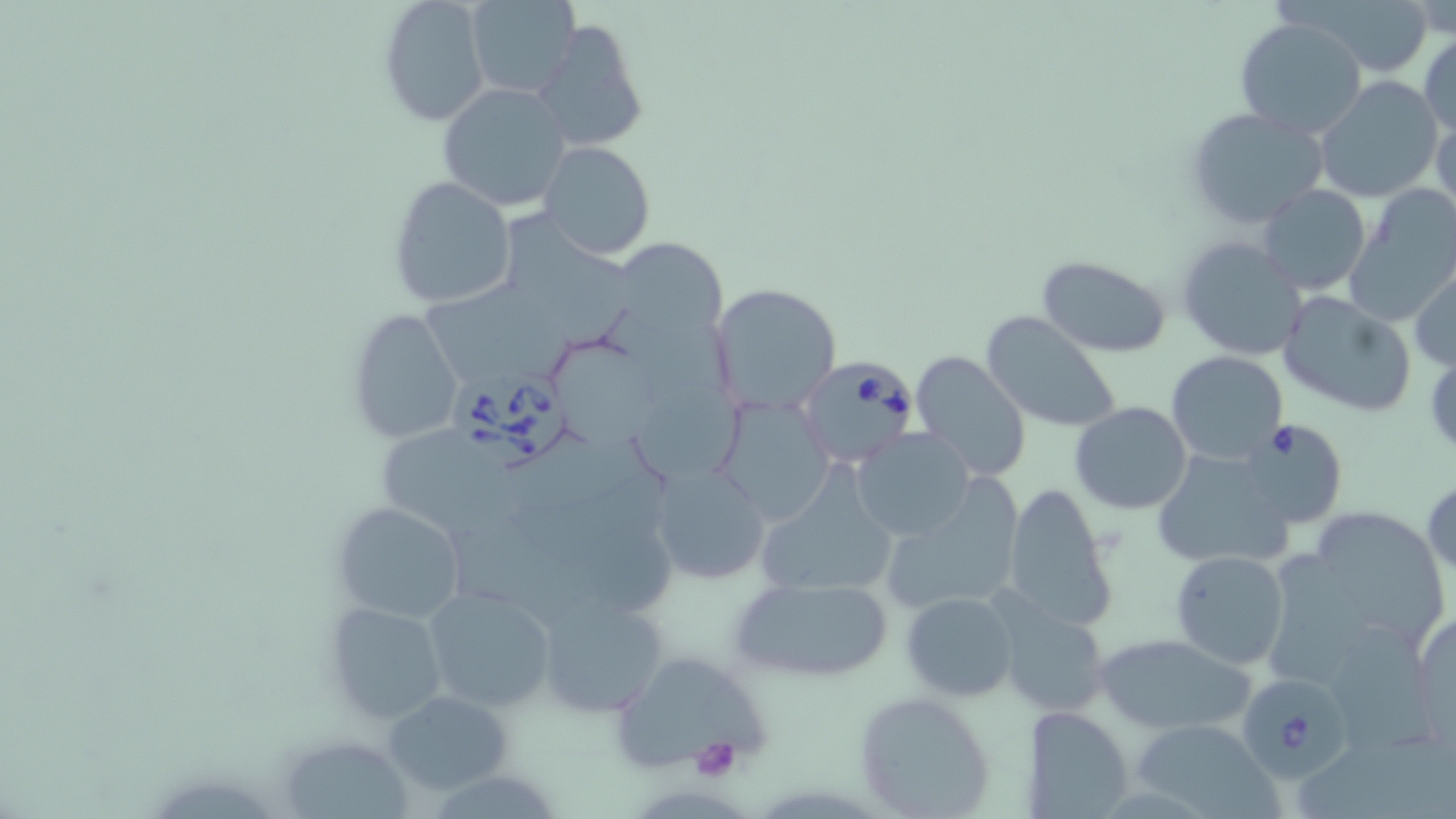
Approximate bounding boxes as [x1, y1, x2, y2] in pixels. Babesia divergens-infected red blood cell locations: [797, 357, 920, 469], [450, 363, 569, 470], [1237, 418, 1347, 529], [1242, 676, 1356, 783]. Platelet locations: [688, 737, 742, 782]. Uninfected red blood cell locations: [376, 0, 492, 127], [465, 0, 578, 98], [1306, 0, 1436, 77], [1234, 17, 1368, 140], [533, 18, 651, 153], [1418, 34, 1455, 140], [1313, 76, 1442, 202], [436, 82, 571, 211], [1187, 107, 1329, 228], [1432, 109, 1456, 222], [537, 140, 655, 260], [388, 176, 517, 308], [1259, 184, 1370, 297], [1345, 188, 1455, 325], [512, 213, 637, 350], [1176, 235, 1308, 361], [620, 237, 727, 338], [1037, 256, 1170, 357], [1410, 264, 1456, 371], [708, 281, 843, 416], [424, 282, 578, 381], [1277, 289, 1416, 418], [346, 307, 465, 444], [605, 309, 737, 410], [980, 310, 1124, 432], [551, 338, 660, 446], [910, 350, 1033, 482], [1167, 351, 1289, 465], [633, 381, 744, 482], [712, 392, 833, 525], [1069, 402, 1193, 516], [385, 428, 525, 530], [851, 429, 977, 541], [1150, 451, 1296, 571], [648, 459, 771, 586], [513, 470, 679, 573], [754, 473, 897, 602], [1422, 478, 1455, 579], [880, 480, 1024, 617], [1002, 483, 1117, 630], [329, 501, 467, 625], [1293, 506, 1448, 649], [448, 516, 590, 622], [1170, 549, 1290, 671], [727, 575, 896, 685], [424, 586, 556, 713], [535, 587, 673, 718], [901, 592, 1019, 701], [323, 599, 452, 727], [993, 601, 1113, 717], [1412, 610, 1455, 740], [1320, 624, 1438, 753], [1095, 633, 1255, 736], [610, 649, 769, 773], [381, 688, 515, 797], [851, 691, 998, 816], [1025, 706, 1132, 817], [1132, 719, 1277, 817], [287, 741, 413, 819]. Slide-level diagnosis: Babesia divergens. Thin blood film. May-Grünwald-Giemsa-stained preparation. Image is 1456×819 pixels. Captured at 1000x magnification. Single field of view. Optical microscopy.